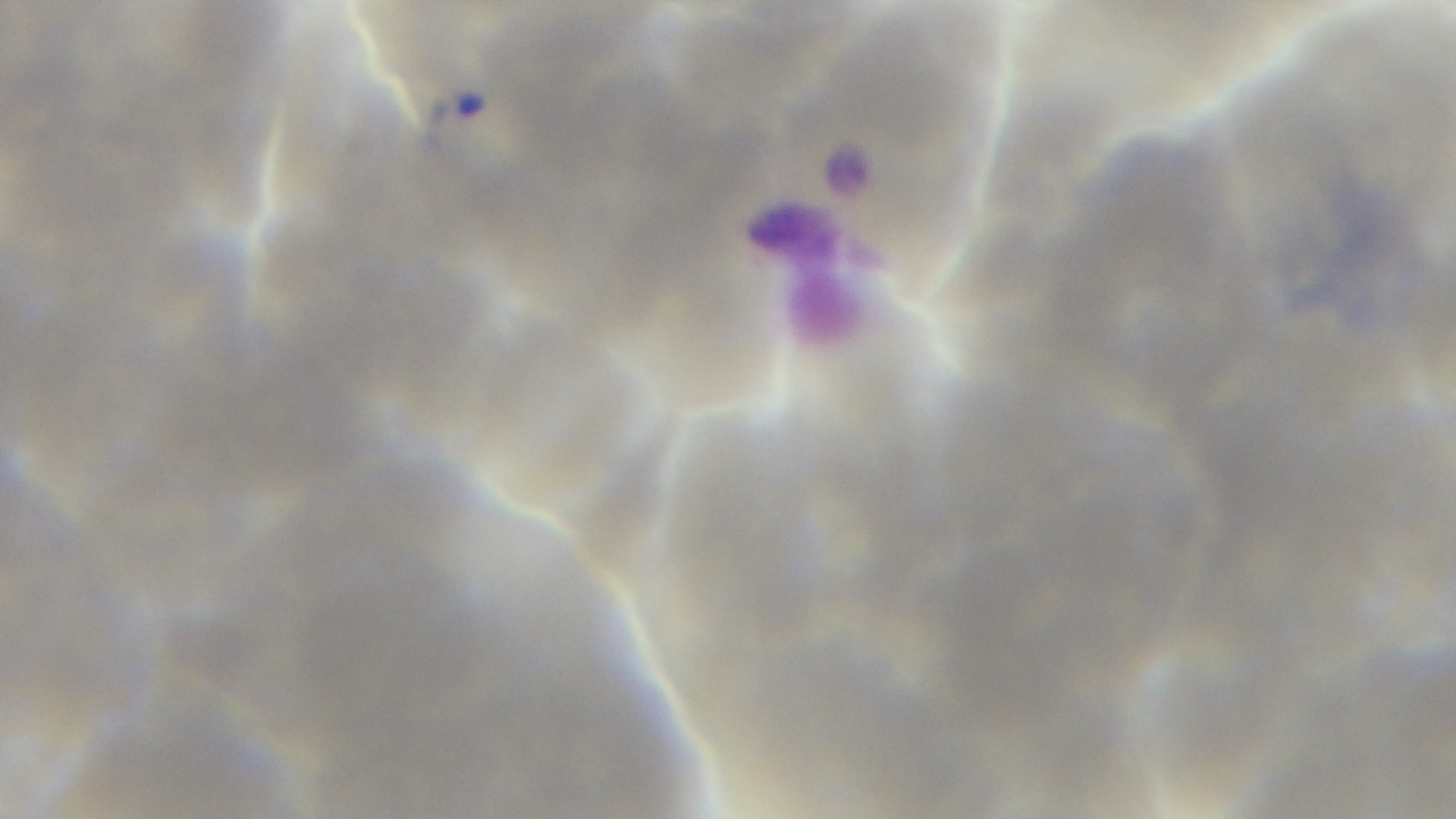

capture: mounted 4K digital camera
preparation: thin
field_of_view: one from the slide
malaria_status: infected
objective: 100x oil immersion
stain: Giemsa
modality: light microscopy